Assess this cell for malaria.
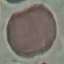
Uninfected.

Summary:
  - Preparation: thin blood smear
  - Capture: smartphone through the microscope eyepiece
  - Stain: Giemsa
  - Image type: automatically extracted cell patch, resized to 64 × 64 pixels